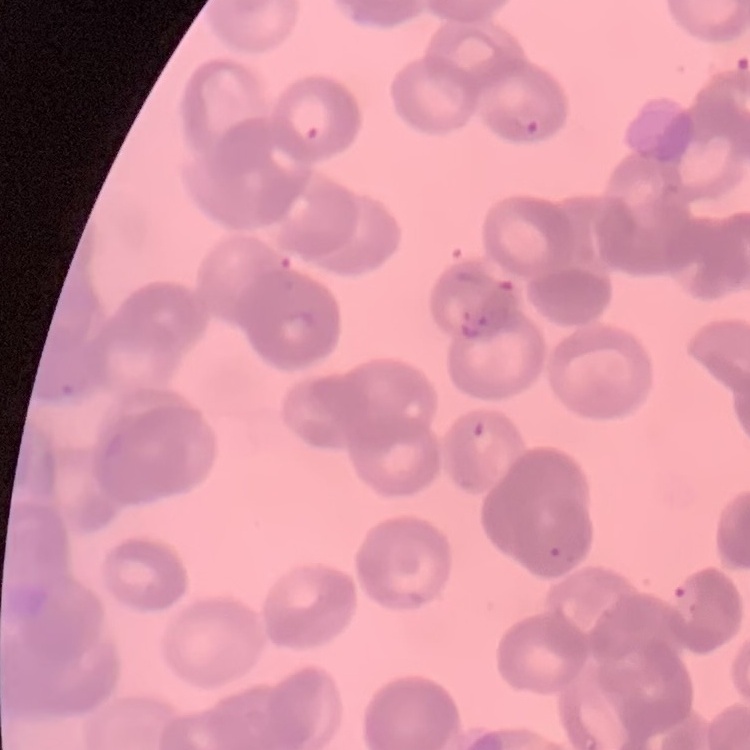
Summary:
  - Erythrocyte morphology: rouleaux formation
  - Preparation: thin blood film
  - Image type: square crop of a larger photomicrograph
  - Stain: Field's or Giemsa